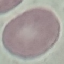

Summary:
  - Malaria status: uninfected
  - Preparation: thin blood film
  - Image type: cell patch, automatically extracted from a larger field of view and resized to 64 × 64 pixels
  - Capture: smartphone through the microscope eyepiece
  - Stain: Giemsa